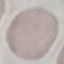
malaria status = uninfected
stain = Giemsa
preparation = thin blood smear
capture = smartphone camera at the microscope eyepiece
image type = automatically extracted cell patch, resized to 64 × 64 pixels